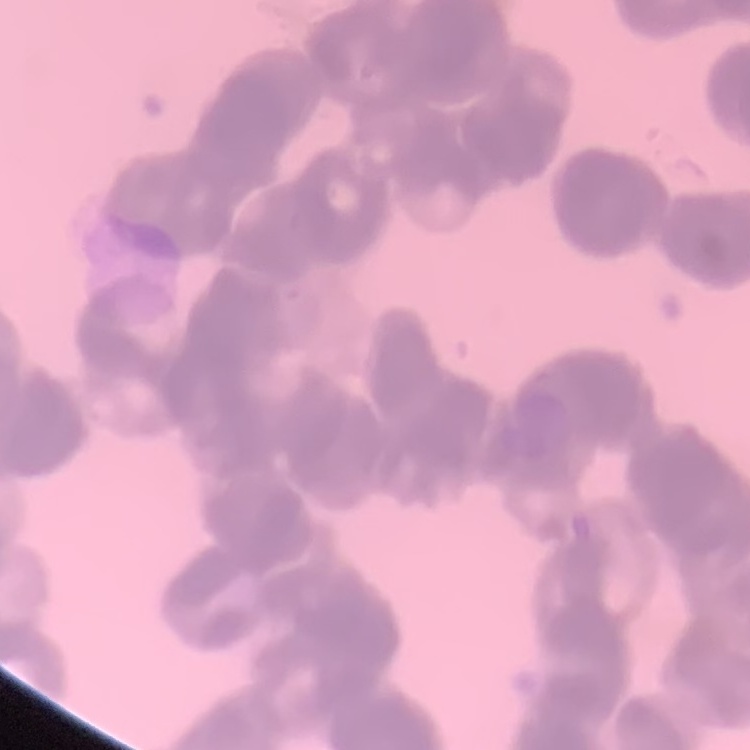 The erythrocytes exhibit rouleaux formation. One tile cut from a larger photomicrograph. Stained with either Field's or Giemsa. Thin blood film.